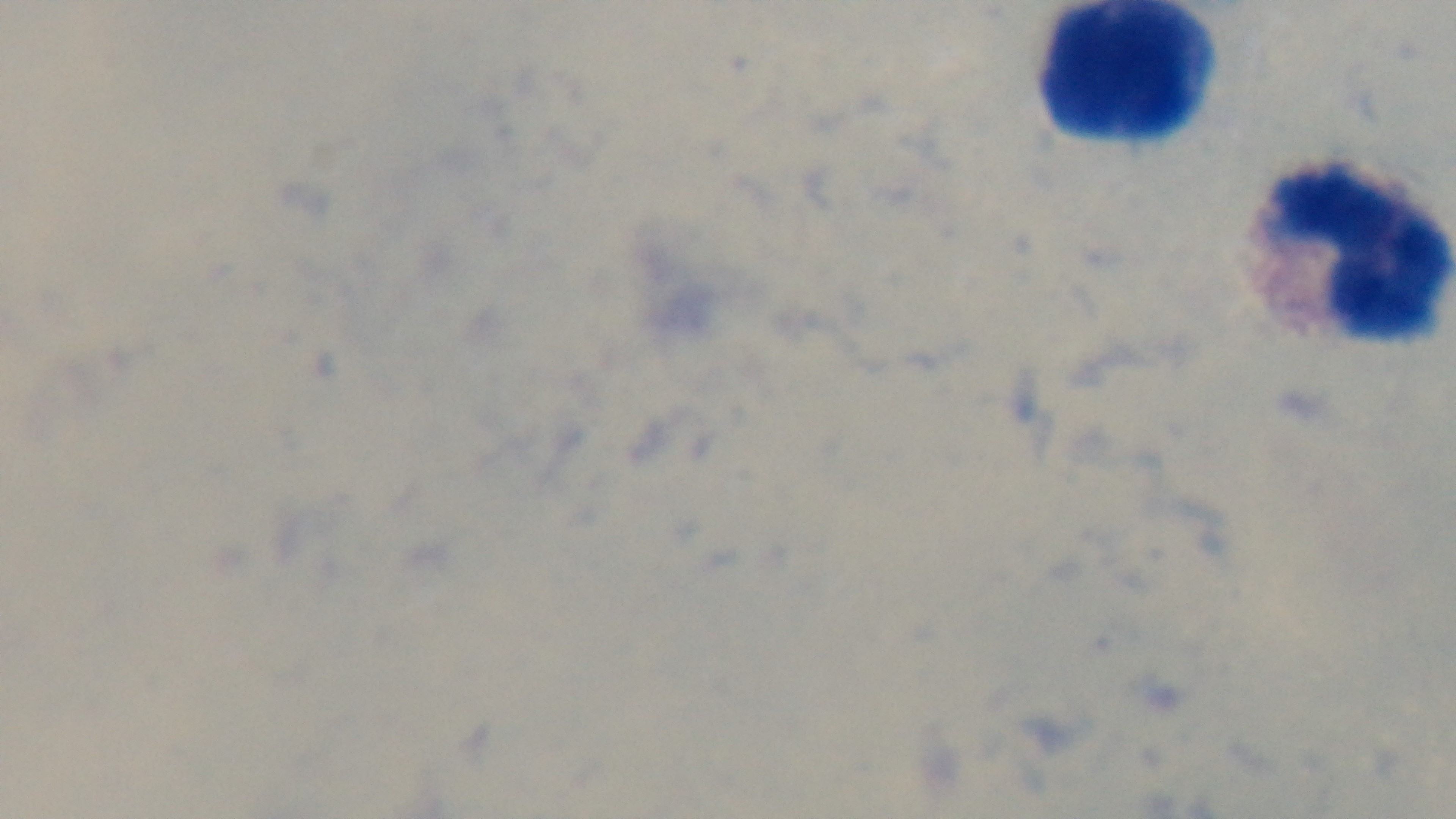

Summary:
  - Field of view: one from the slide
  - Preparation: thick
  - Objective: 100x oil immersion
  - Capture: mounted 4K digital camera
  - Malaria status: uninfected
  - Stain: Giemsa
  - Modality: light microscopy